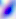

magnification = 400x
modality = micrograph
identification = Toxoplasma gondii